Report the malaria status of this cell.
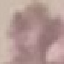

Uninfected.

{
  "image_type": "automatically extracted cell patch, resized to 64 × 64 pixels",
  "capture": "smartphone through the microscope eyepiece",
  "preparation": "thin blood smear",
  "stain": "Giemsa"
}